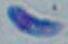 Toxoplasma gondii is seen. Micrograph. Captured at 1000x magnification.